Report the malaria status of this cell.
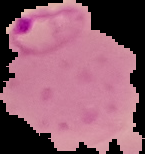
Parasitized.

Summary:
  - Image size: 145×154 pixels
  - Preparation: thin blood film
  - Image type: cell region segmented out of the field of view; surrounding area masked to black